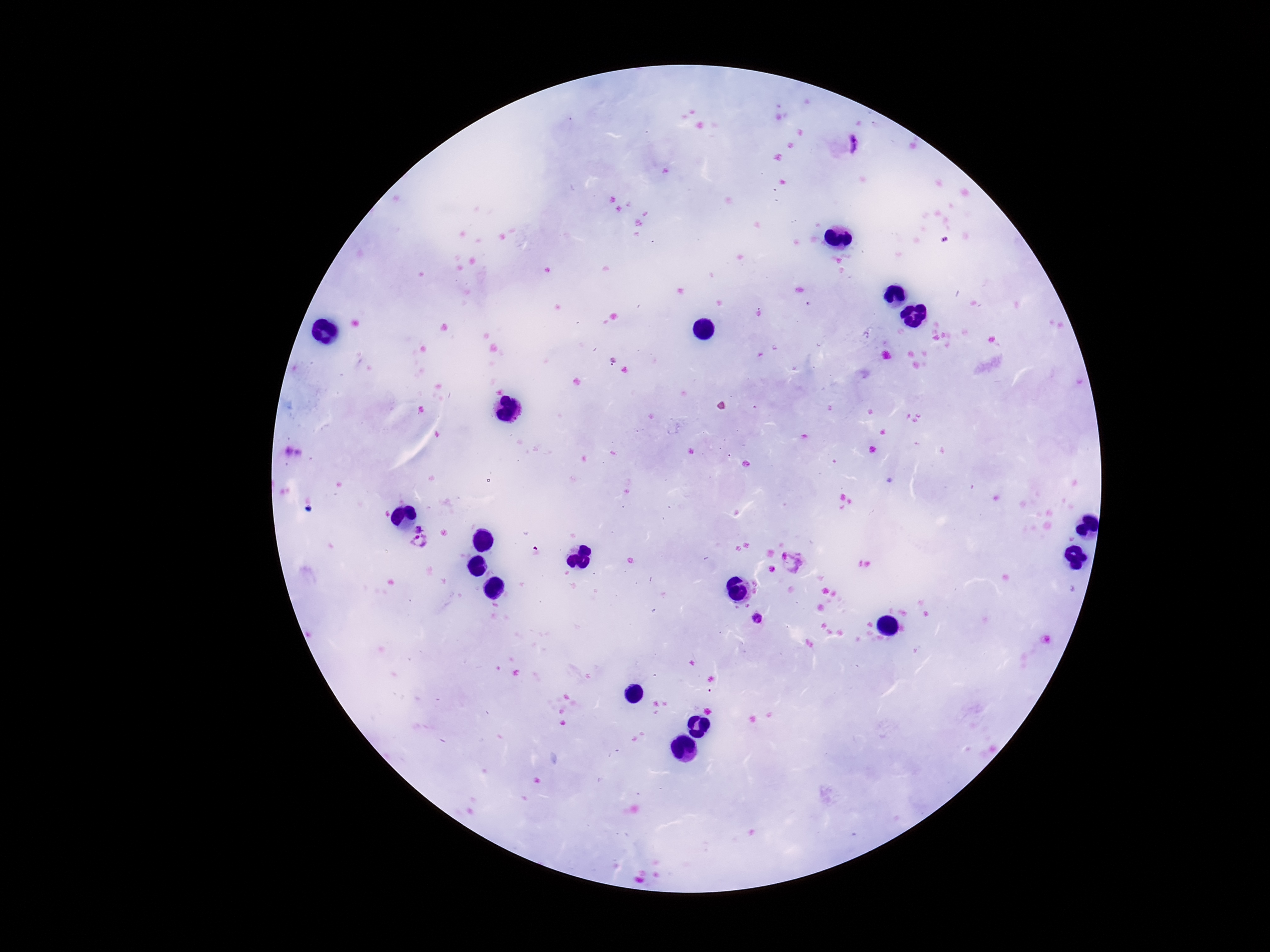

Approximate centers as [x, y] in pixels.
Summary:
  - Plasmodium parasite locations: [854, 144], [421, 526], [417, 543], [795, 562], [757, 619]
  - Capture: smartphone camera through the microscope eyepiece
  - Field of view: one from this slide
  - Stain: Giemsa
  - Image size: 1270×952 pixels
  - Patient malaria status: infected
  - Magnification: 100x
  - Preparation: thick blood smear